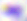
Photomicrograph. Toxoplasma gondii is shown. Captured at 400x magnification.